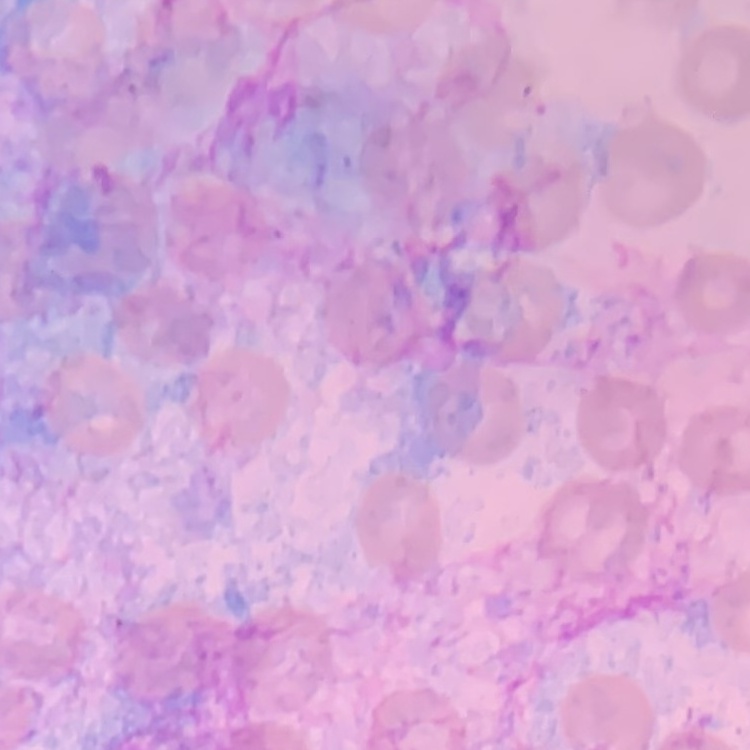

Summary:
  - Erythrocyte morphology: no rouleaux formation
  - Stain: Field's or Giemsa
  - Image type: one tile cut from a larger photomicrograph
  - Preparation: thin peripheral smear